Point out every malaria parasite.
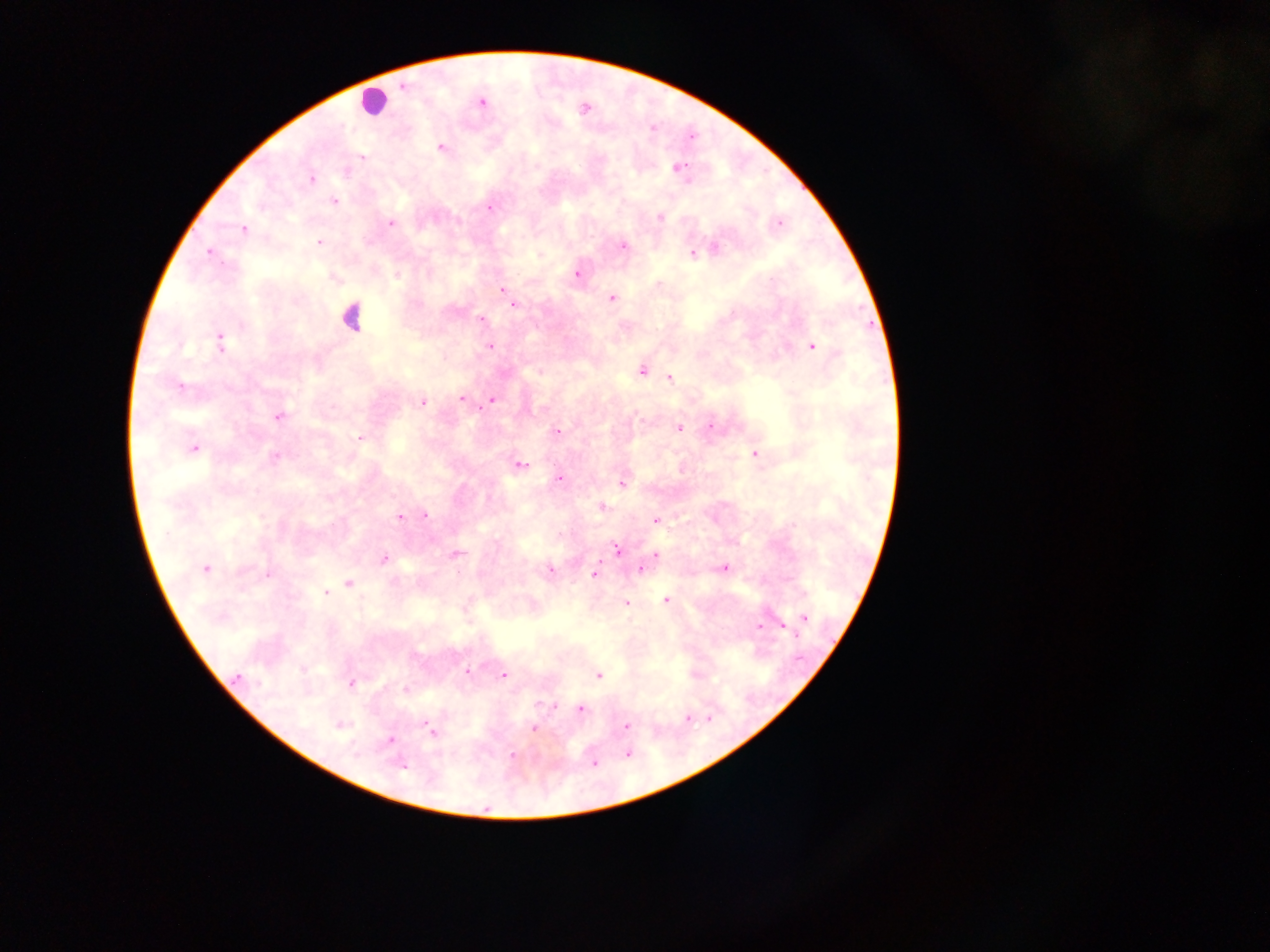
Approximate centers as {x, y} in pixels.
Malaria parasites: {481, 102}, {440, 147}, {362, 157}, {677, 168}, {311, 179}, {334, 200}, {489, 207}, {660, 217}, {391, 223}, {778, 224}, {243, 229}, {319, 242}, {622, 245}, {714, 248}, {208, 251}, {706, 251}, {693, 253}, {576, 273}, {503, 290}, {611, 298}, {513, 305}, {481, 319}, {219, 342}, {489, 345}, {812, 345}, {641, 369}, {669, 378}, {179, 387}, {462, 399}, {491, 400}, {422, 401}, {279, 415}, {711, 424}, {678, 428}, {556, 431}, {359, 438}, {193, 448}, {754, 454}, {273, 456}, {517, 465}, {559, 479}, {622, 483}, {600, 506}, {425, 515}, {400, 517}, {655, 519}, {617, 549}, {454, 554}, {655, 554}, {384, 558}, {639, 567}, {204, 568}, {723, 568}, {549, 570}, {268, 573}, {594, 573}, {348, 583}, {326, 593}, {665, 600}, {626, 602}, {805, 617}, {781, 624}, {758, 627}, {467, 672}, {502, 675}, {597, 675}, {350, 683}, {405, 689}, {579, 709}, {687, 717}, {340, 724}, {625, 726}, {533, 728}, {430, 732}, {390, 740}, {628, 753}, {512, 755}, {593, 763}, {399, 765}.

Summary:
  - Leukocyte locations: {373, 101}, {351, 316}
  - Capture: mobile-phone photograph through a microscope
  - Preparation: thick blood smear
  - Country: Ghana
  - Image size: 1270×952 pixels
  - Field of view: single